Give the location of every parasitized red blood cell.
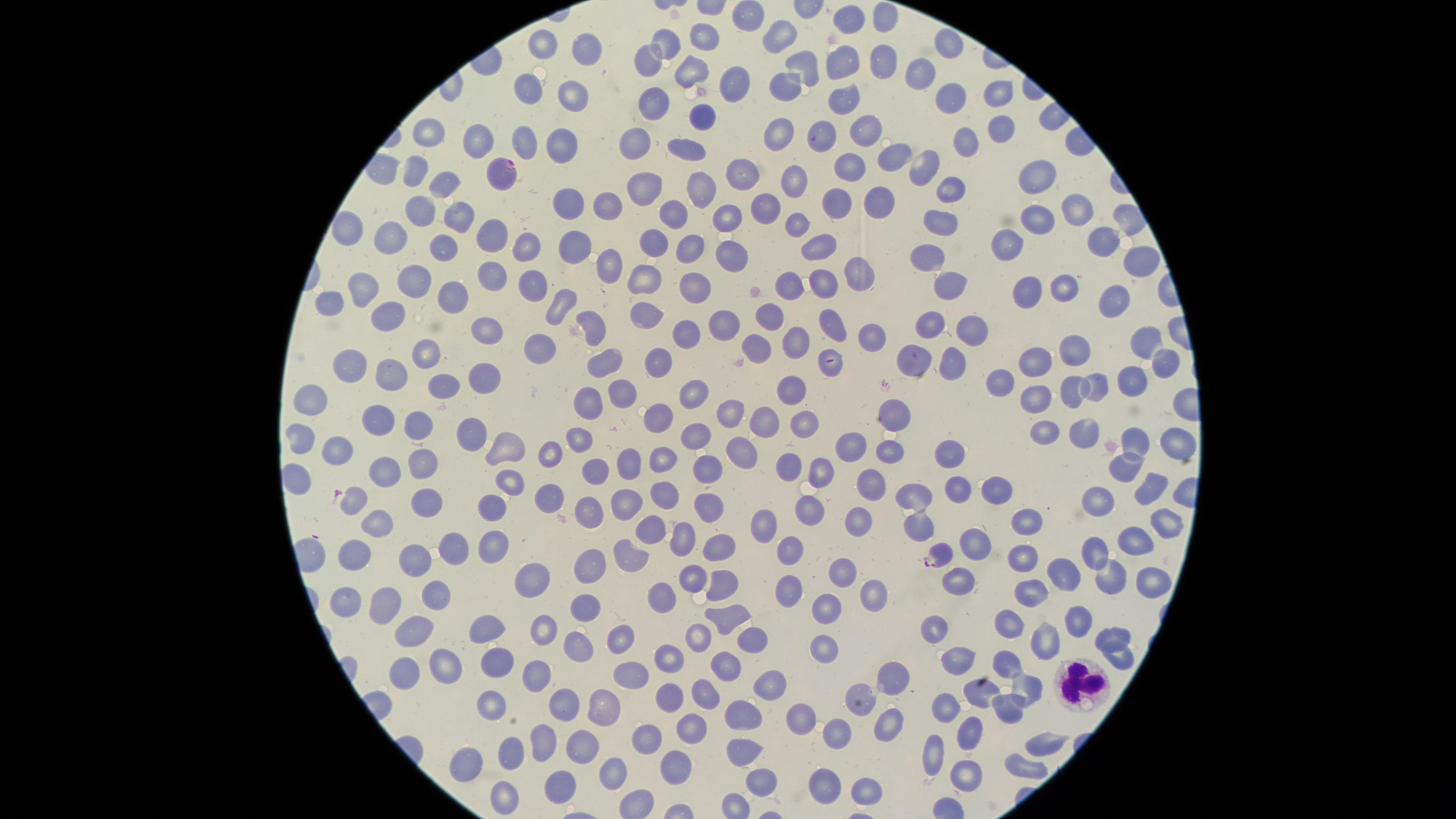
Approximate marker points as (x, y) in pixels.
Parasitized red blood cells: (498, 176), (937, 555).

{
  "field_of_view": "single",
  "uninfected_red_blood_cells": "approximate marker points as (x, y) in pixels: (744, 15), (881, 17), (851, 23), (706, 40), (782, 40), (667, 41), (944, 42), (540, 45), (576, 54), (644, 59), (878, 59), (840, 63), (687, 69), (805, 69), (922, 76), (727, 81), (782, 84), (995, 93), (525, 94), (574, 96), (945, 96), (842, 101), (655, 103), (698, 117), (996, 125), (823, 129), (862, 130), (426, 131), (774, 131), (479, 139), (639, 142), (523, 143), (562, 143), (961, 143), (686, 147), (895, 155), (415, 165), (848, 167), (921, 167), (743, 173), (1038, 177), (792, 179), (442, 183), (645, 186), (705, 186), (946, 189), (569, 200), (608, 203), (880, 203), (765, 204), (840, 204), (417, 205), (1076, 210), (670, 212), (1043, 218), (453, 219), (724, 219), (801, 222), (936, 223), (342, 228), (486, 235), (391, 240), (1008, 240), (1102, 243), (658, 244), (689, 244), (823, 244), (443, 245), (575, 246), (521, 248), (729, 252), (929, 259), (1135, 264), (610, 267), (855, 273), (641, 274), (494, 277), (946, 279), (787, 282), (529, 283), (1060, 284), (691, 285), (826, 285), (411, 286), (1019, 286), (364, 287), (452, 294), (563, 294), (332, 297), (1112, 301), (386, 319), (651, 319), (772, 321), (835, 323), (723, 325), (930, 325), (683, 329), (483, 330), (867, 330), (593, 331), (969, 334), (1141, 334), (801, 339), (759, 341), (539, 346), (914, 354), (1076, 354), (427, 355), (658, 355), (948, 360), (1028, 361), (601, 364), (347, 365), (1159, 365), (833, 367), (390, 373), (1005, 378), (1131, 380), (483, 381), (443, 386), (620, 388), (1097, 388), (694, 390), (790, 390), (311, 394), (1038, 394), (1070, 396), (587, 398), (894, 406), (731, 415), (373, 418), (657, 419), (798, 421), (414, 423), (763, 423), (1050, 428), (1086, 429), (471, 433), (575, 436), (1135, 438), (299, 441), (846, 444), (512, 446), (1174, 446), (739, 449), (550, 452), (948, 452), (892, 453), (341, 455), (658, 459), (422, 461), (790, 464), (631, 468), (823, 468), (702, 469), (383, 470), (1124, 470), (292, 474), (511, 476), (594, 476), (868, 479), (993, 485), (952, 487), (664, 490), (1146, 492), (545, 494), (912, 495), (1095, 498), (419, 499), (358, 501), (624, 501), (706, 504), (494, 509), (809, 512), (589, 516), (374, 517), (1024, 518), (856, 519), (1160, 522), (763, 523), (918, 523), (647, 526), (687, 530), (455, 535), (712, 541), (972, 541), (1134, 543), (492, 546), (788, 547), (631, 551), (1097, 551), (357, 559), (409, 559), (1023, 559), (599, 563), (840, 571), (1068, 573), (1150, 574), (1110, 576), (523, 578), (690, 578), (961, 580), (727, 582), (870, 587), (1039, 589), (786, 590), (665, 591), (345, 595), (431, 601), (375, 604), (587, 604), (826, 607), (1079, 619), (721, 620), (1006, 620), (541, 621), (493, 622), (937, 625), (413, 629), (620, 631), (749, 635), (1113, 636), (1050, 640), (583, 641), (697, 642), (823, 648), (963, 651), (667, 656), (1118, 656), (1003, 661), (732, 662), (449, 666), (495, 667), (630, 669), (400, 671), (535, 677), (891, 679), (772, 681), (1028, 685), (983, 689), (703, 692), (669, 693), (859, 694), (565, 703), (603, 703), (945, 708), (1004, 708), (488, 709), (800, 709), (741, 717), (888, 719), (690, 727), (836, 731), (976, 733), (645, 737), (583, 738), (542, 739), (1038, 743), (738, 754), (936, 754), (508, 757), (467, 758), (676, 765), (615, 769), (1022, 769), (968, 775), (754, 779), (556, 781), (826, 784), (869, 789), (500, 793)",
  "image_size": "1456×819 pixels",
  "stain": "Giemsa",
  "white_blood_cells": "approximate marker points as (x, y) in pixels: (1080, 684)",
  "capture": "smartphone photograph through the microscope eyepiece",
  "species": "Plasmodium falciparum",
  "visible_region": "circular",
  "preparation": "thin blood smear"
}